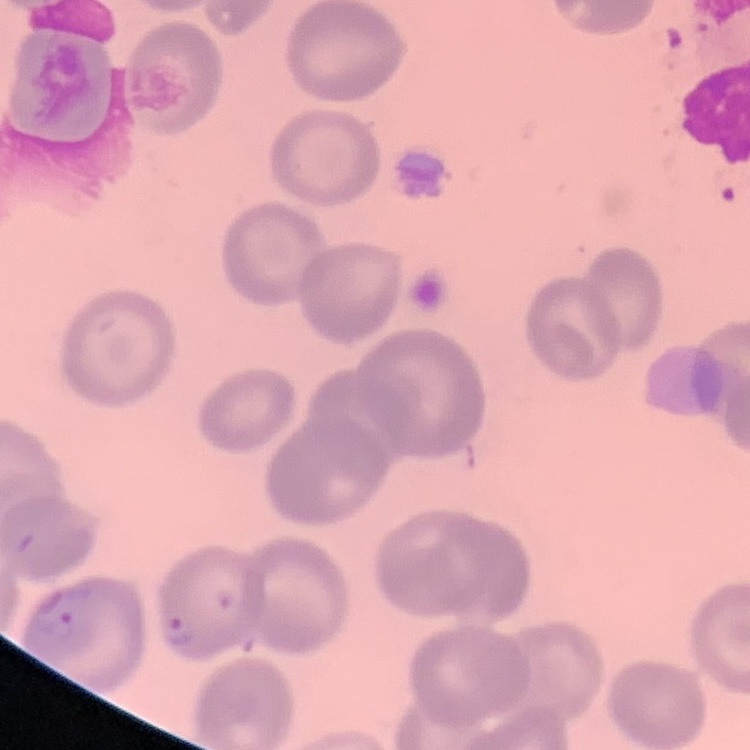

Summary:
  - Red blood cell morphology: no rouleaux formation
  - Preparation: thin blood film
  - Image type: square crop of a larger photomicrograph
  - Stain: Field's or Giemsa